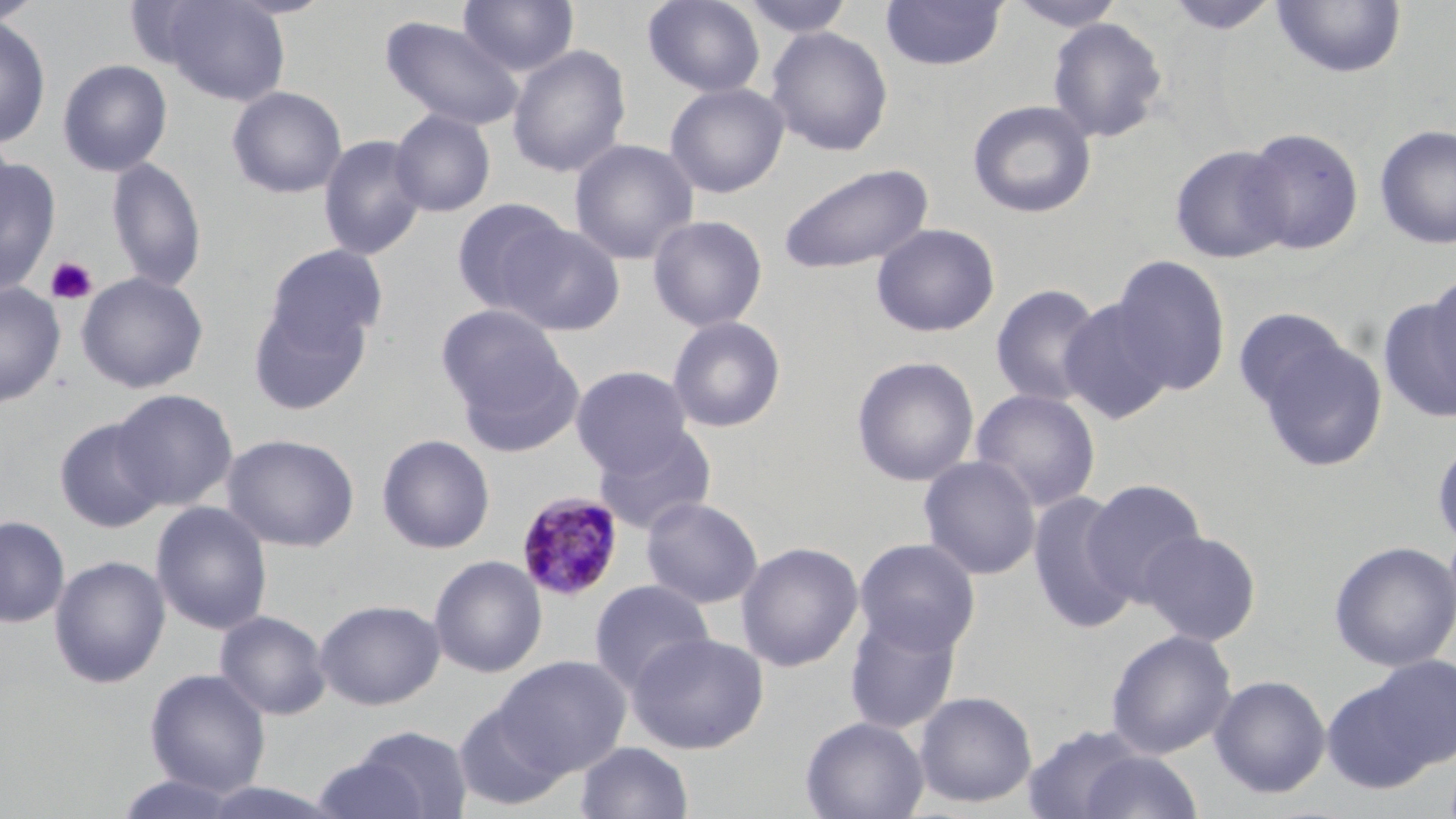

Summary:
  - Coordinate format: approximate bounding boxes as named x1/y1/x2/y2 corners in pixels
  - Uninfected red blood cell locations: (x1=0, y1=0, x2=45, y2=26), (x1=154, y1=0, x2=292, y2=106), (x1=457, y1=0, x2=580, y2=76), (x1=642, y1=0, x2=766, y2=97), (x1=879, y1=0, x2=1007, y2=72), (x1=1005, y1=0, x2=1128, y2=31), (x1=1164, y1=0, x2=1281, y2=35), (x1=738, y1=1, x2=857, y2=39), (x1=1271, y1=1, x2=1407, y2=79), (x1=0, y1=14, x2=51, y2=150), (x1=381, y1=15, x2=524, y2=131), (x1=1046, y1=17, x2=1168, y2=143), (x1=765, y1=26, x2=894, y2=156), (x1=506, y1=45, x2=631, y2=178), (x1=57, y1=59, x2=173, y2=177), (x1=665, y1=82, x2=789, y2=198), (x1=226, y1=86, x2=347, y2=199), (x1=967, y1=99, x2=1097, y2=219), (x1=389, y1=109, x2=497, y2=217), (x1=1374, y1=124, x2=1456, y2=250), (x1=1240, y1=127, x2=1365, y2=255), (x1=318, y1=134, x2=428, y2=260), (x1=569, y1=138, x2=699, y2=265), (x1=1170, y1=145, x2=1292, y2=264), (x1=0, y1=155, x2=61, y2=297), (x1=106, y1=156, x2=207, y2=293), (x1=776, y1=163, x2=934, y2=276), (x1=451, y1=197, x2=572, y2=314), (x1=647, y1=214, x2=768, y2=332), (x1=499, y1=221, x2=625, y2=335), (x1=871, y1=223, x2=1000, y2=338), (x1=264, y1=244, x2=388, y2=354), (x1=1111, y1=254, x2=1231, y2=396), (x1=75, y1=272, x2=209, y2=394), (x1=1423, y1=272, x2=1456, y2=404), (x1=0, y1=282, x2=66, y2=407), (x1=990, y1=283, x2=1105, y2=409), (x1=248, y1=296, x2=371, y2=416), (x1=1377, y1=297, x2=1456, y2=422), (x1=1059, y1=298, x2=1176, y2=424), (x1=436, y1=304, x2=567, y2=415), (x1=667, y1=315, x2=787, y2=433), (x1=1247, y1=328, x2=1388, y2=473), (x1=456, y1=350, x2=583, y2=457), (x1=851, y1=356, x2=980, y2=487), (x1=570, y1=365, x2=694, y2=476), (x1=969, y1=387, x2=1101, y2=511), (x1=111, y1=389, x2=238, y2=510), (x1=54, y1=417, x2=168, y2=533), (x1=592, y1=424, x2=718, y2=536), (x1=222, y1=433, x2=360, y2=552), (x1=376, y1=434, x2=495, y2=554), (x1=1431, y1=435, x2=1456, y2=551), (x1=918, y1=455, x2=1041, y2=580), (x1=1082, y1=478, x2=1208, y2=604), (x1=1027, y1=490, x2=1139, y2=634), (x1=640, y1=497, x2=763, y2=608), (x1=151, y1=501, x2=273, y2=635), (x1=0, y1=516, x2=70, y2=628), (x1=1138, y1=529, x2=1262, y2=646), (x1=854, y1=537, x2=981, y2=655), (x1=1329, y1=540, x2=1456, y2=672), (x1=736, y1=542, x2=863, y2=672), (x1=429, y1=554, x2=547, y2=678), (x1=49, y1=555, x2=170, y2=689), (x1=589, y1=580, x2=714, y2=692), (x1=314, y1=598, x2=446, y2=710), (x1=214, y1=609, x2=332, y2=721), (x1=844, y1=610, x2=963, y2=736), (x1=1105, y1=629, x2=1237, y2=760), (x1=628, y1=632, x2=769, y2=754), (x1=496, y1=656, x2=631, y2=776), (x1=1326, y1=660, x2=1455, y2=790), (x1=144, y1=668, x2=271, y2=797), (x1=1209, y1=674, x2=1331, y2=798), (x1=914, y1=690, x2=1038, y2=808), (x1=452, y1=702, x2=570, y2=812), (x1=800, y1=716, x2=928, y2=819), (x1=1022, y1=724, x2=1150, y2=818), (x1=348, y1=725, x2=474, y2=819), (x1=576, y1=741, x2=693, y2=819), (x1=1077, y1=751, x2=1203, y2=819), (x1=310, y1=755, x2=434, y2=819), (x1=112, y1=773, x2=247, y2=818)
  - Platelet locations: (x1=46, y1=257, x2=98, y2=306)
  - Plasmodium malariae-infected red blood cell locations: (x1=516, y1=491, x2=625, y2=601)
  - Slide-level diagnosis: Plasmodium malariae
  - Field of view: one of a larger specimen
  - Preparation: thin blood smear
  - Stain: May-Grünwald-Giemsa
  - Magnification: 1000x
  - Image size: 1456×819 pixels
  - Modality: light microscopy